Locate and identify every blood parasite.
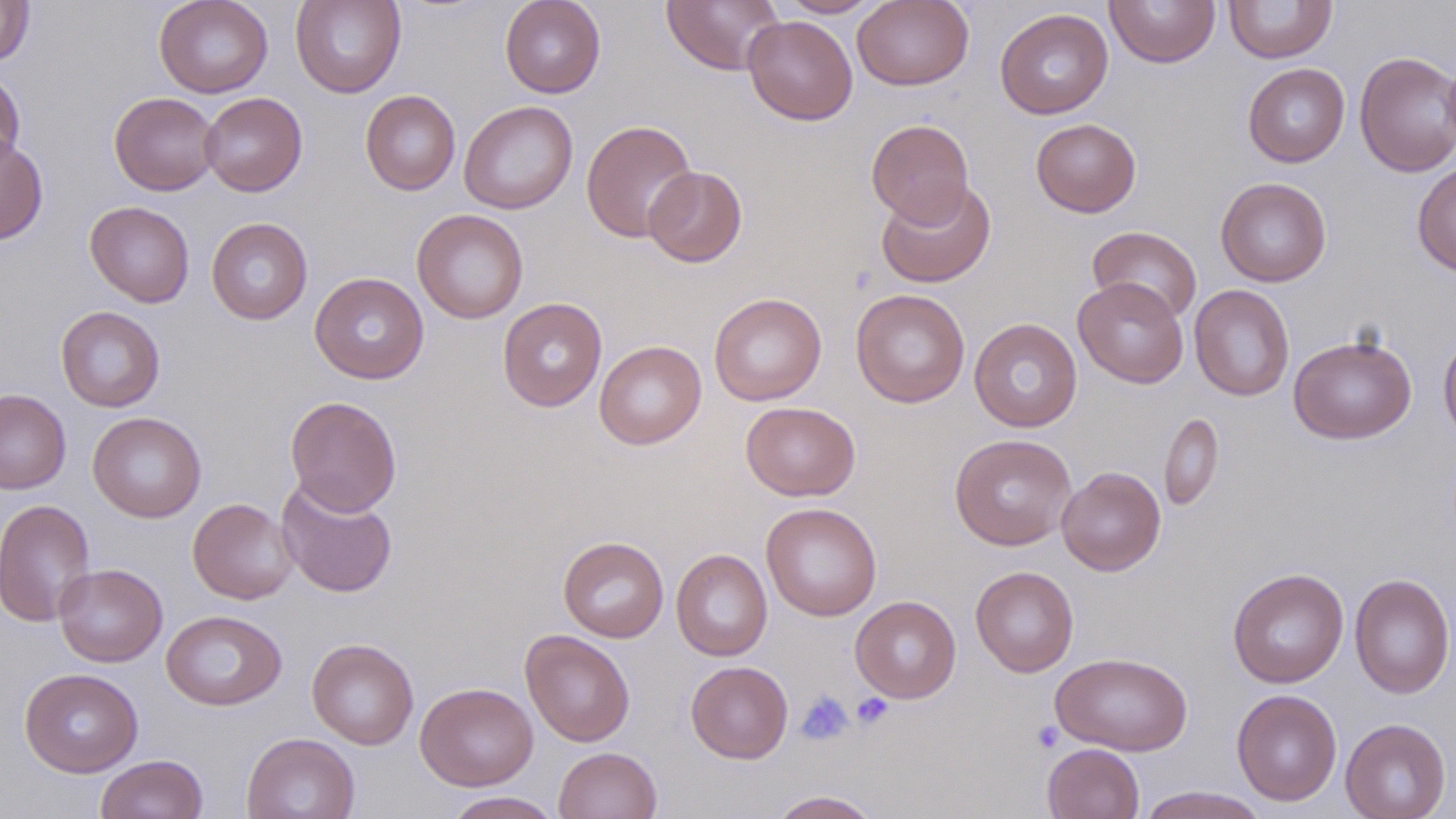

No blood parasites observed.

Summary:
  - Coordinate format: approximate bounding boxes as named x1/y1/x2/y2 corners in pixels
  - Platelet locations: (x1=796, y1=691, x2=853, y2=745), (x1=851, y1=693, x2=894, y2=730), (x1=1031, y1=720, x2=1065, y2=753)
  - Uninfected red blood cell locations: (x1=154, y1=0, x2=273, y2=98), (x1=290, y1=0, x2=407, y2=98), (x1=500, y1=0, x2=606, y2=98), (x1=662, y1=0, x2=783, y2=75), (x1=776, y1=0, x2=882, y2=18), (x1=852, y1=0, x2=974, y2=90), (x1=1104, y1=0, x2=1220, y2=67), (x1=1223, y1=1, x2=1337, y2=63), (x1=0, y1=2, x2=35, y2=66), (x1=995, y1=8, x2=1113, y2=119), (x1=743, y1=15, x2=858, y2=125), (x1=1354, y1=50, x2=1456, y2=177), (x1=1243, y1=63, x2=1350, y2=167), (x1=0, y1=69, x2=26, y2=174), (x1=360, y1=90, x2=461, y2=195), (x1=109, y1=92, x2=221, y2=196), (x1=199, y1=92, x2=307, y2=196), (x1=459, y1=100, x2=578, y2=214), (x1=866, y1=118, x2=975, y2=227), (x1=1030, y1=118, x2=1142, y2=217), (x1=581, y1=120, x2=699, y2=243), (x1=0, y1=134, x2=49, y2=246), (x1=1412, y1=161, x2=1456, y2=277), (x1=643, y1=165, x2=747, y2=267), (x1=1215, y1=177, x2=1332, y2=287), (x1=876, y1=179, x2=996, y2=288), (x1=84, y1=200, x2=195, y2=307), (x1=412, y1=209, x2=528, y2=324), (x1=206, y1=217, x2=313, y2=324), (x1=1087, y1=226, x2=1202, y2=324), (x1=309, y1=272, x2=429, y2=384), (x1=1073, y1=277, x2=1189, y2=388), (x1=1189, y1=284, x2=1294, y2=401), (x1=851, y1=288, x2=970, y2=407), (x1=708, y1=292, x2=827, y2=406), (x1=497, y1=297, x2=607, y2=412), (x1=55, y1=306, x2=165, y2=412), (x1=969, y1=318, x2=1082, y2=432), (x1=1438, y1=332, x2=1456, y2=447), (x1=1288, y1=335, x2=1417, y2=444), (x1=594, y1=340, x2=707, y2=450), (x1=0, y1=389, x2=71, y2=494), (x1=285, y1=396, x2=402, y2=516), (x1=740, y1=401, x2=860, y2=501), (x1=88, y1=411, x2=207, y2=523), (x1=1159, y1=412, x2=1223, y2=512), (x1=949, y1=434, x2=1078, y2=551), (x1=1056, y1=466, x2=1166, y2=576), (x1=276, y1=477, x2=397, y2=598), (x1=188, y1=498, x2=297, y2=604), (x1=0, y1=499, x2=96, y2=626), (x1=760, y1=502, x2=882, y2=621), (x1=558, y1=536, x2=669, y2=642), (x1=671, y1=548, x2=773, y2=661), (x1=54, y1=563, x2=167, y2=667), (x1=970, y1=566, x2=1079, y2=677), (x1=1227, y1=568, x2=1349, y2=688), (x1=1350, y1=573, x2=1455, y2=699), (x1=850, y1=596, x2=962, y2=703), (x1=161, y1=609, x2=287, y2=711), (x1=520, y1=629, x2=635, y2=747), (x1=307, y1=638, x2=419, y2=749), (x1=1050, y1=651, x2=1193, y2=755), (x1=685, y1=661, x2=793, y2=763), (x1=19, y1=668, x2=143, y2=777), (x1=415, y1=682, x2=538, y2=790), (x1=1232, y1=688, x2=1342, y2=806), (x1=1340, y1=717, x2=1451, y2=819), (x1=241, y1=732, x2=360, y2=819), (x1=1042, y1=743, x2=1144, y2=819), (x1=553, y1=746, x2=662, y2=819), (x1=95, y1=753, x2=209, y2=818), (x1=1133, y1=786, x2=1269, y2=818), (x1=767, y1=790, x2=883, y2=818), (x1=443, y1=791, x2=563, y2=818)
  - Slide-level diagnosis: negative for blood parasites
  - Image size: 1456×819 pixels
  - Modality: optical microscopy
  - Field of view: one of a larger specimen
  - Magnification: 1000x
  - Preparation: thin blood smear
  - Stain: May-Grünwald-Giemsa